Locate every white blood cell.
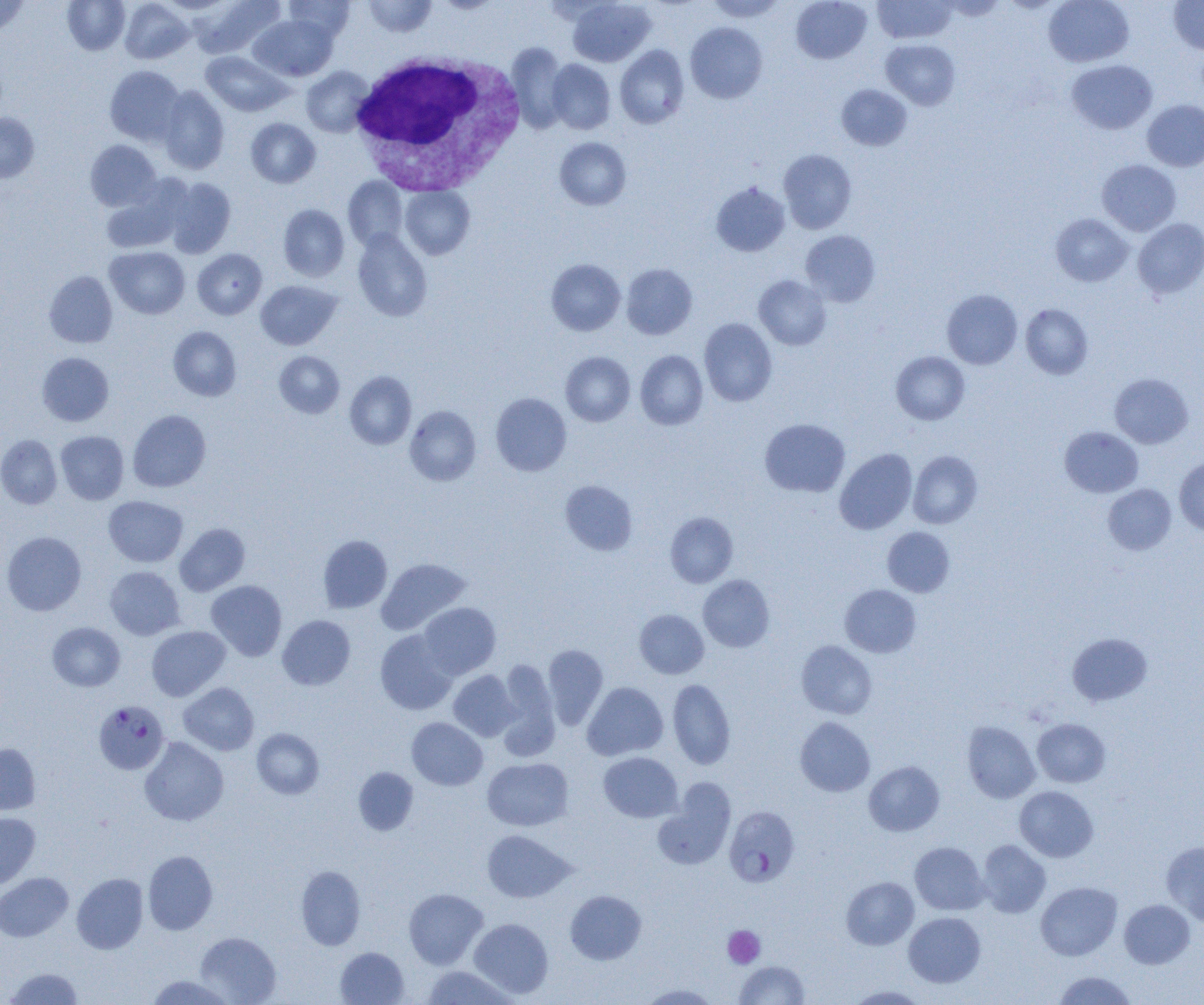

Approximate bounding boxes as named x1/y1/x2/y2 corners in pixels.
White blood cells: (x1=349, y1=50, x2=526, y2=195).

Uninfected red blood cell locations: (x1=0, y1=0, x2=30, y2=38), (x1=62, y1=0, x2=130, y2=54), (x1=119, y1=0, x2=195, y2=64), (x1=192, y1=0, x2=285, y2=58), (x1=283, y1=0, x2=355, y2=42), (x1=362, y1=0, x2=437, y2=37), (x1=433, y1=0, x2=503, y2=13), (x1=567, y1=0, x2=656, y2=67), (x1=705, y1=0, x2=785, y2=22), (x1=791, y1=0, x2=871, y2=64), (x1=873, y1=0, x2=957, y2=43), (x1=1043, y1=0, x2=1134, y2=67), (x1=1169, y1=1, x2=1204, y2=53), (x1=249, y1=14, x2=337, y2=81), (x1=685, y1=22, x2=767, y2=103), (x1=881, y1=39, x2=960, y2=110), (x1=506, y1=43, x2=569, y2=133), (x1=615, y1=45, x2=689, y2=128), (x1=201, y1=51, x2=291, y2=117), (x1=547, y1=59, x2=615, y2=134), (x1=1066, y1=59, x2=1157, y2=134), (x1=105, y1=65, x2=185, y2=146), (x1=301, y1=66, x2=374, y2=137), (x1=836, y1=84, x2=912, y2=151), (x1=157, y1=86, x2=230, y2=174), (x1=1143, y1=100, x2=1204, y2=171), (x1=0, y1=113, x2=39, y2=182), (x1=246, y1=118, x2=321, y2=188), (x1=555, y1=137, x2=631, y2=210), (x1=85, y1=140, x2=160, y2=211), (x1=778, y1=149, x2=857, y2=233), (x1=1097, y1=159, x2=1181, y2=236), (x1=342, y1=177, x2=408, y2=250), (x1=165, y1=178, x2=236, y2=258), (x1=100, y1=181, x2=187, y2=254), (x1=711, y1=182, x2=790, y2=257), (x1=400, y1=186, x2=474, y2=260), (x1=278, y1=204, x2=350, y2=281), (x1=1051, y1=213, x2=1133, y2=287), (x1=1133, y1=218, x2=1204, y2=298), (x1=352, y1=229, x2=432, y2=321), (x1=800, y1=230, x2=880, y2=307), (x1=105, y1=246, x2=190, y2=318), (x1=193, y1=248, x2=267, y2=319), (x1=546, y1=259, x2=626, y2=336), (x1=621, y1=263, x2=697, y2=339), (x1=44, y1=271, x2=118, y2=348), (x1=754, y1=275, x2=831, y2=350), (x1=256, y1=280, x2=341, y2=350), (x1=941, y1=289, x2=1022, y2=369), (x1=1020, y1=303, x2=1093, y2=379), (x1=699, y1=318, x2=777, y2=406), (x1=168, y1=326, x2=242, y2=400), (x1=635, y1=350, x2=708, y2=429), (x1=274, y1=351, x2=345, y2=418), (x1=561, y1=351, x2=635, y2=426), (x1=891, y1=351, x2=970, y2=424), (x1=37, y1=352, x2=114, y2=426), (x1=345, y1=371, x2=417, y2=450), (x1=1109, y1=373, x2=1193, y2=448), (x1=491, y1=392, x2=571, y2=476), (x1=404, y1=405, x2=481, y2=486), (x1=128, y1=410, x2=211, y2=492), (x1=760, y1=418, x2=850, y2=497), (x1=1060, y1=426, x2=1143, y2=497), (x1=55, y1=431, x2=129, y2=504), (x1=0, y1=434, x2=62, y2=509), (x1=835, y1=448, x2=917, y2=534), (x1=908, y1=450, x2=983, y2=528), (x1=1174, y1=457, x2=1204, y2=536), (x1=560, y1=480, x2=637, y2=555), (x1=1103, y1=484, x2=1176, y2=555), (x1=103, y1=495, x2=188, y2=567), (x1=665, y1=512, x2=738, y2=587), (x1=174, y1=523, x2=250, y2=596), (x1=882, y1=526, x2=955, y2=596), (x1=1, y1=531, x2=86, y2=616), (x1=318, y1=535, x2=392, y2=613), (x1=376, y1=558, x2=472, y2=635), (x1=105, y1=566, x2=185, y2=640), (x1=698, y1=575, x2=774, y2=652), (x1=206, y1=580, x2=287, y2=661), (x1=840, y1=585, x2=921, y2=657), (x1=418, y1=602, x2=500, y2=679), (x1=635, y1=609, x2=708, y2=679), (x1=277, y1=615, x2=356, y2=690), (x1=47, y1=622, x2=125, y2=691), (x1=147, y1=626, x2=230, y2=700), (x1=375, y1=629, x2=458, y2=715), (x1=1068, y1=633, x2=1152, y2=705), (x1=796, y1=641, x2=877, y2=719), (x1=543, y1=644, x2=608, y2=730), (x1=497, y1=659, x2=559, y2=756), (x1=448, y1=670, x2=519, y2=741), (x1=667, y1=679, x2=736, y2=769), (x1=178, y1=682, x2=259, y2=755), (x1=582, y1=682, x2=668, y2=760), (x1=406, y1=717, x2=487, y2=790), (x1=795, y1=717, x2=875, y2=796), (x1=1032, y1=718, x2=1110, y2=787), (x1=962, y1=721, x2=1040, y2=803), (x1=252, y1=728, x2=324, y2=799), (x1=139, y1=737, x2=229, y2=826), (x1=0, y1=743, x2=41, y2=815), (x1=599, y1=752, x2=683, y2=822), (x1=482, y1=757, x2=574, y2=831), (x1=864, y1=761, x2=944, y2=836), (x1=354, y1=768, x2=419, y2=835), (x1=654, y1=780, x2=735, y2=870), (x1=1014, y1=785, x2=1098, y2=862), (x1=0, y1=813, x2=40, y2=890), (x1=481, y1=830, x2=575, y2=903), (x1=977, y1=840, x2=1051, y2=918), (x1=1162, y1=841, x2=1204, y2=925), (x1=910, y1=842, x2=989, y2=915), (x1=143, y1=850, x2=217, y2=935), (x1=296, y1=865, x2=366, y2=949), (x1=0, y1=872, x2=73, y2=942), (x1=72, y1=873, x2=149, y2=954), (x1=841, y1=876, x2=919, y2=950), (x1=1035, y1=881, x2=1122, y2=960), (x1=404, y1=888, x2=488, y2=969), (x1=565, y1=890, x2=646, y2=964), (x1=1119, y1=899, x2=1195, y2=968), (x1=904, y1=912, x2=986, y2=987), (x1=469, y1=918, x2=553, y2=998), (x1=195, y1=932, x2=281, y2=1004), (x1=335, y1=947, x2=409, y2=1004), (x1=735, y1=960, x2=809, y2=1004), (x1=421, y1=965, x2=518, y2=1004), (x1=3, y1=967, x2=84, y2=1004), (x1=1053, y1=971, x2=1137, y2=1004), (x1=145, y1=975, x2=236, y2=1005), (x1=639, y1=983, x2=720, y2=1004), (x1=845, y1=985, x2=930, y2=1004). Platelet locations: (x1=723, y1=925, x2=765, y2=968). Plasmodium falciparum-infected red blood cell locations: (x1=94, y1=700, x2=169, y2=775), (x1=724, y1=806, x2=800, y2=886). Slide-level diagnosis: Plasmodium falciparum. One field of a larger specimen. Optical microscopy. Image is 1204×1005 pixels. Thin blood film. 1000x magnification.